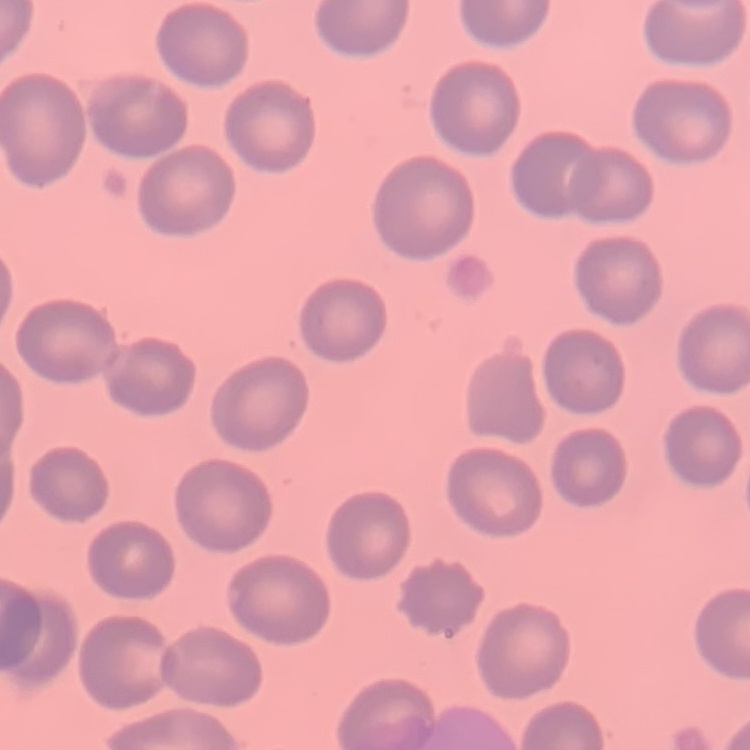 The erythrocytes exhibit no rouleaux formation. Square crop of a larger photomicrograph. Thin peripheral smear. Stained with either Field's or Giemsa.